Assess this cell for malaria.
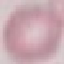
It is uninfected.

stain = Giemsa
image type = cell patch, automatically extracted from a larger field of view and resized to 64 × 64 pixels
preparation = thin smear
capture = smartphone through the microscope eyepiece